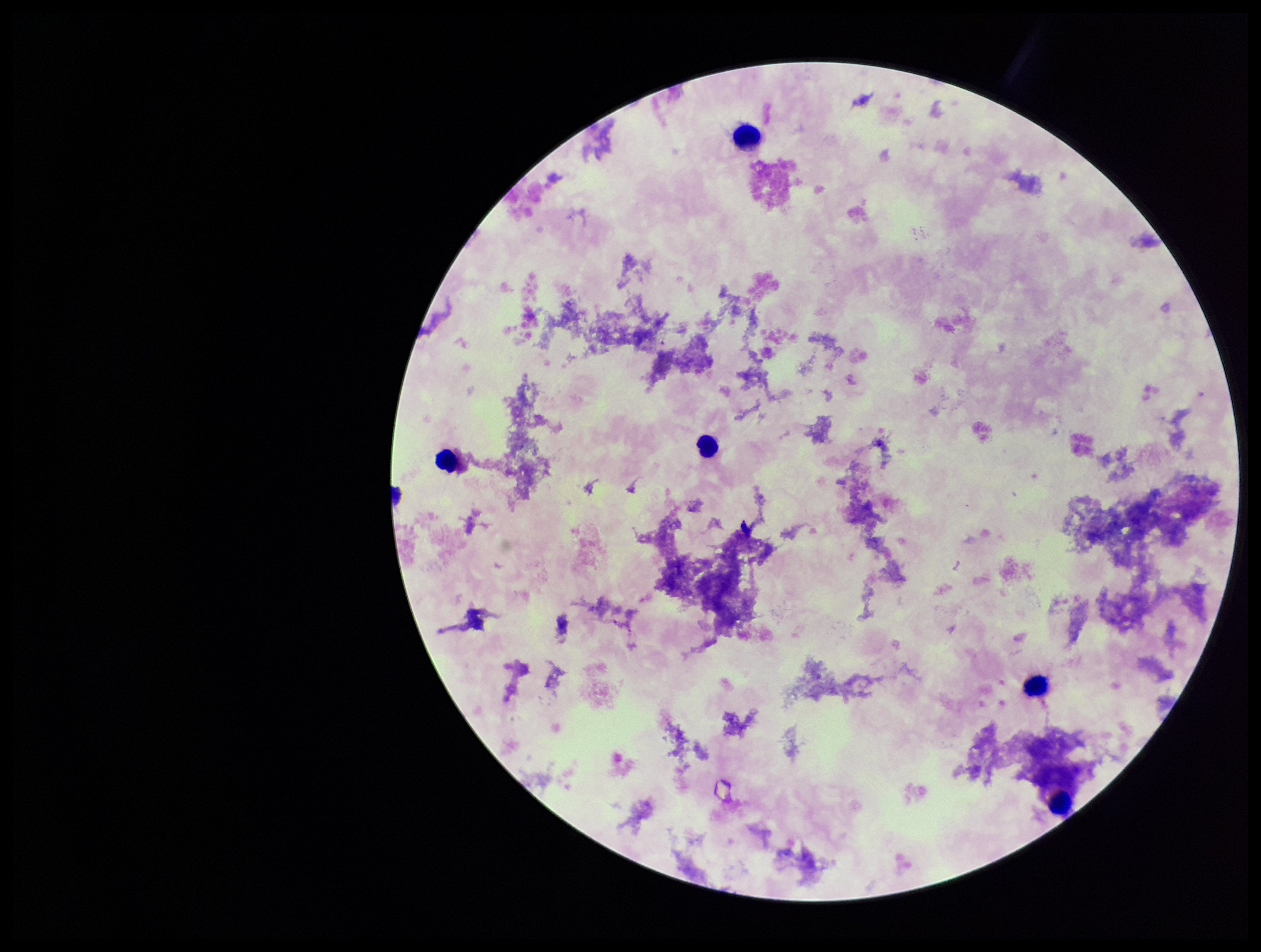

capture = smartphone photograph through the microscope eyepiece
Plasmodium parasites = none identified
preparation = thick smear
leukocyte count = 5
stain = Giemsa
field of view = single
parasite count = 0
patient malaria status = negative
image size = 1261×952 pixels